Classify this cell by malaria status.
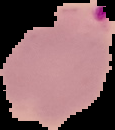
Parasitized.

preparation = thin blood smear
image size = 115×130 pixels
image type = segmented cell region with the area outside set to black